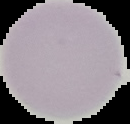
preparation: thin blood smear
result: negative for Plasmodium parasites
image_size: 130×124 pixels
image_type: segmented cell region on a black background